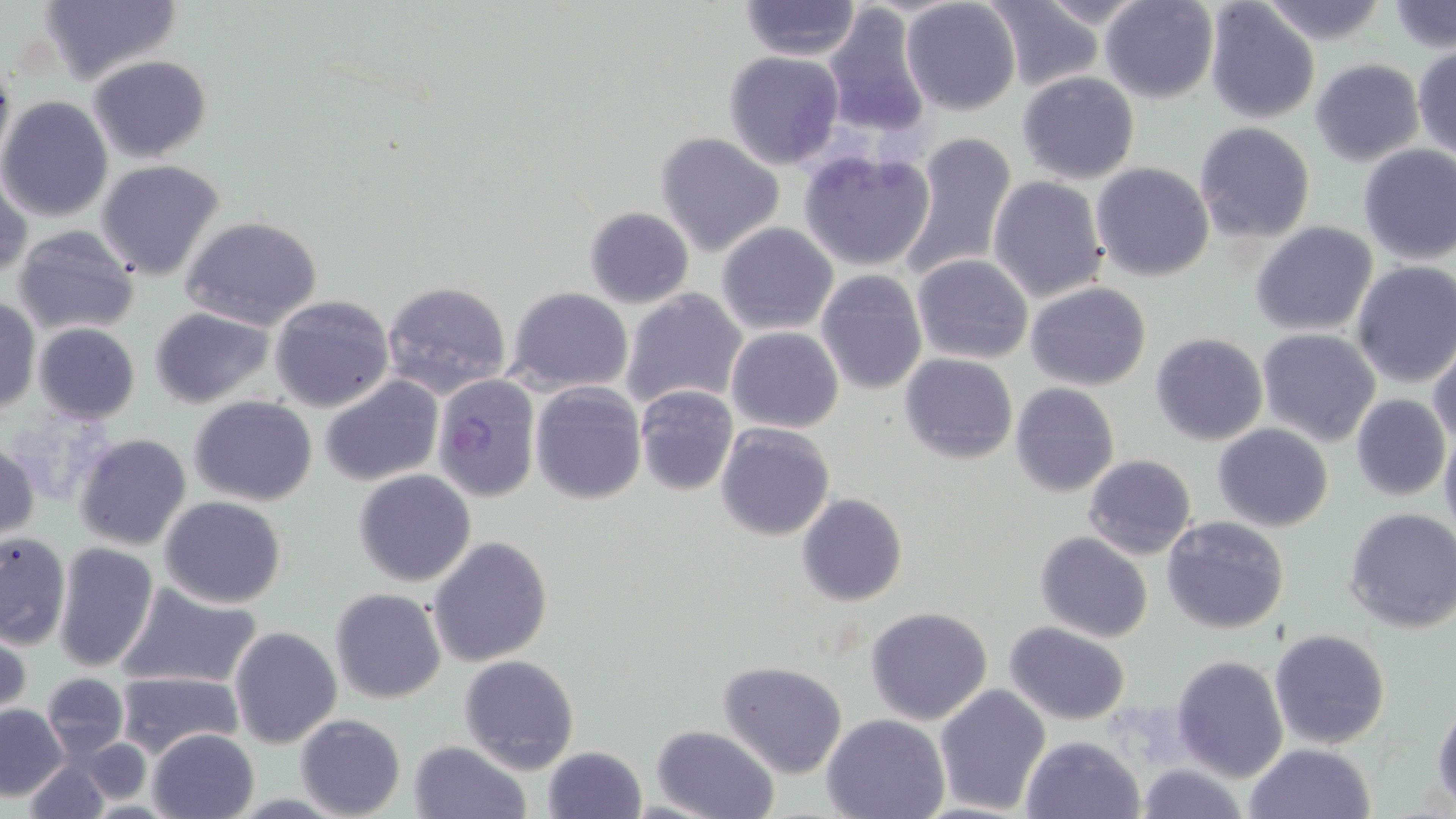

Summary:
  - Coordinate format: approximate bounding boxes as [x1, y1, x2, y2] in pixels
  - Uninfected red blood cell locations: [38, 0, 182, 86], [982, 0, 1107, 91], [1099, 0, 1219, 104], [739, 1, 860, 58], [901, 1, 1020, 115], [1205, 1, 1320, 122], [1260, 1, 1390, 46], [822, 2, 933, 139], [1389, 3, 1454, 53], [1413, 43, 1456, 158], [724, 51, 846, 170], [88, 54, 212, 163], [1309, 59, 1424, 167], [0, 61, 15, 177], [1017, 71, 1140, 184], [0, 96, 114, 222], [1193, 122, 1315, 244], [655, 131, 786, 258], [896, 131, 1018, 281], [1357, 144, 1455, 265], [797, 149, 937, 274], [97, 159, 225, 282], [1091, 162, 1214, 282], [1, 167, 30, 282], [988, 176, 1107, 302], [583, 206, 695, 310], [180, 215, 325, 331], [1250, 221, 1379, 336], [716, 222, 838, 335], [11, 224, 142, 337], [911, 254, 1033, 364], [1352, 261, 1456, 388], [813, 268, 928, 395], [382, 281, 512, 398], [1025, 282, 1151, 390], [505, 288, 633, 392], [621, 288, 748, 411], [269, 295, 395, 411], [1, 297, 39, 417], [150, 307, 274, 408], [32, 323, 140, 423], [726, 327, 845, 433], [1257, 327, 1381, 446], [1150, 332, 1269, 445], [1429, 345, 1456, 452], [899, 353, 1017, 464], [320, 375, 442, 485], [531, 382, 647, 504], [1010, 382, 1119, 497], [634, 387, 737, 497], [1351, 393, 1452, 500], [189, 395, 318, 505], [715, 423, 835, 541], [1212, 424, 1334, 531], [1440, 425, 1456, 541], [74, 433, 192, 550], [0, 440, 40, 541], [1084, 453, 1197, 558], [354, 469, 475, 585], [795, 493, 908, 607], [160, 496, 287, 609], [1343, 507, 1456, 633], [1161, 516, 1290, 636], [0, 531, 70, 647], [1035, 532, 1154, 642], [428, 534, 552, 666], [51, 543, 160, 673], [117, 583, 264, 689], [331, 588, 446, 703], [865, 606, 992, 724], [1, 622, 31, 721], [1004, 622, 1131, 724], [229, 626, 342, 747], [1269, 629, 1392, 749], [459, 654, 579, 772], [1172, 654, 1288, 780], [718, 660, 848, 778], [113, 670, 244, 758], [42, 673, 129, 759], [934, 683, 1050, 813], [1431, 701, 1456, 809], [0, 705, 69, 798], [296, 713, 405, 819], [821, 714, 948, 819], [651, 724, 778, 819], [147, 728, 257, 818], [1020, 734, 1144, 819], [76, 737, 157, 806], [407, 740, 532, 819], [1243, 744, 1376, 819], [541, 746, 647, 819], [24, 760, 108, 818], [1132, 761, 1249, 819]
  - Plasmodium falciparum-infected red blood cell locations: [431, 373, 541, 499]
  - Slide-level diagnosis: Plasmodium falciparum
  - Field of view: one of a larger specimen
  - Magnification: 1000x
  - Image size: 1456×819 pixels
  - Modality: light microscopy
  - Stain: May-Grünwald-Giemsa
  - Preparation: thin blood film